State which parasite is depicted.
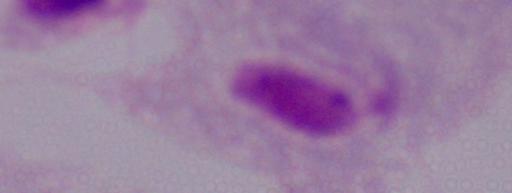

This is a trichomonad.

modality = micrograph
magnification = 1000x